Classify this cell by malaria status.
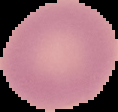

Uninfected.

Summary:
  - Image type: segmented cell region with the area outside set to black
  - Image size: 118×112 pixels
  - Preparation: thin blood film